Locate every blood parasite and identify its species.
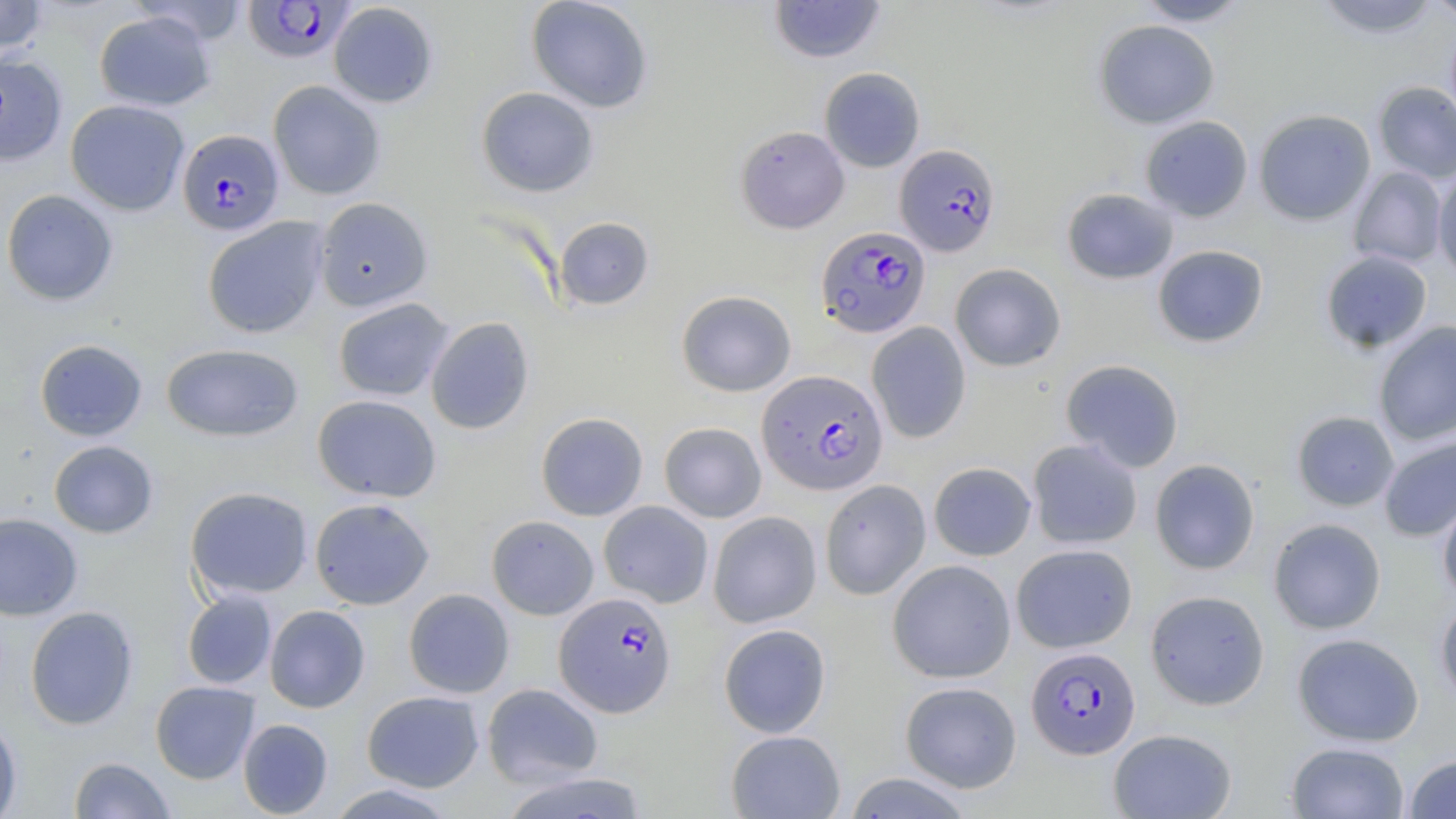

Approximate bounding boxes as (x1, y1, x2, y2) in pixels.
Plasmodium falciparum-infected red blood cells: (242, 1, 356, 63), (177, 128, 285, 236), (895, 144, 1001, 256), (816, 226, 931, 338), (757, 369, 888, 495), (554, 591, 677, 717), (1026, 646, 1141, 759).
No Plasmodium ovale, Plasmodium malariae, Plasmodium vivax, Babesia divergens, or Trypanosoma brucei observed.

Uninfected red blood cell locations: (0, 0, 51, 57), (526, 0, 654, 113), (768, 0, 886, 63), (1133, 0, 1252, 26), (1312, 0, 1443, 38), (1424, 0, 1456, 24), (328, 2, 439, 108), (93, 11, 216, 111), (1445, 17, 1456, 132), (1093, 20, 1219, 129), (0, 53, 67, 166), (819, 67, 925, 172), (268, 80, 386, 200), (1373, 81, 1456, 184), (476, 86, 600, 197), (65, 99, 189, 216), (1253, 109, 1376, 225), (1140, 116, 1253, 222), (736, 125, 849, 233), (1348, 166, 1448, 268), (1433, 170, 1456, 280), (1061, 188, 1179, 284), (1, 189, 119, 307), (314, 197, 434, 312), (202, 216, 329, 339), (554, 216, 654, 311), (1152, 244, 1269, 348), (1320, 250, 1432, 353), (949, 263, 1066, 372), (676, 290, 796, 396), (332, 297, 454, 401), (425, 316, 535, 435), (1373, 321, 1456, 446), (866, 322, 972, 444), (33, 339, 148, 442), (161, 343, 305, 442), (1060, 359, 1184, 473), (311, 394, 442, 503), (1291, 411, 1399, 511), (536, 412, 648, 521), (659, 422, 767, 523), (1379, 435, 1456, 542), (1027, 439, 1143, 549), (48, 440, 159, 539), (1149, 458, 1260, 575), (928, 462, 1036, 561), (819, 479, 931, 600), (185, 486, 314, 601), (1438, 490, 1456, 605), (309, 498, 435, 609), (598, 501, 714, 608), (707, 510, 822, 628), (0, 512, 84, 621), (486, 515, 599, 620), (1268, 518, 1386, 634), (1011, 543, 1137, 653), (887, 559, 1017, 683), (403, 588, 515, 698), (1145, 589, 1270, 710), (182, 590, 277, 690), (1435, 598, 1456, 707), (24, 605, 139, 730), (264, 605, 370, 713), (718, 623, 831, 738), (1292, 633, 1424, 746), (150, 680, 260, 784), (899, 681, 1022, 793), (482, 683, 603, 788), (361, 690, 484, 792), (0, 715, 22, 819), (238, 718, 334, 818), (1108, 728, 1237, 818), (726, 729, 845, 818), (1286, 742, 1410, 819), (1404, 754, 1456, 818), (68, 757, 175, 819), (497, 770, 650, 818), (842, 772, 975, 819), (325, 783, 459, 818). Slide-level diagnosis: Plasmodium falciparum. Image is 1456×819 pixels. May-Grünwald-Giemsa stain. Captured at 1000x magnification. Thin blood smear. Optical microscopy. Single field of view.